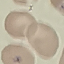

Summary:
  - Malaria status: uninfected
  - Stain: Giemsa
  - Preparation: thin blood film
  - Image type: cell patch, automatically extracted from a larger field of view and resized to 64 × 64 pixels
  - Capture: smartphone camera at the microscope eyepiece